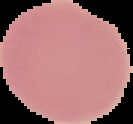
Summary:
  - Result: no Plasmodium parasites detected
  - Image size: 133×124 pixels
  - Preparation: thin blood smear
  - Image type: cell region segmented out of the field of view; surrounding area masked to black